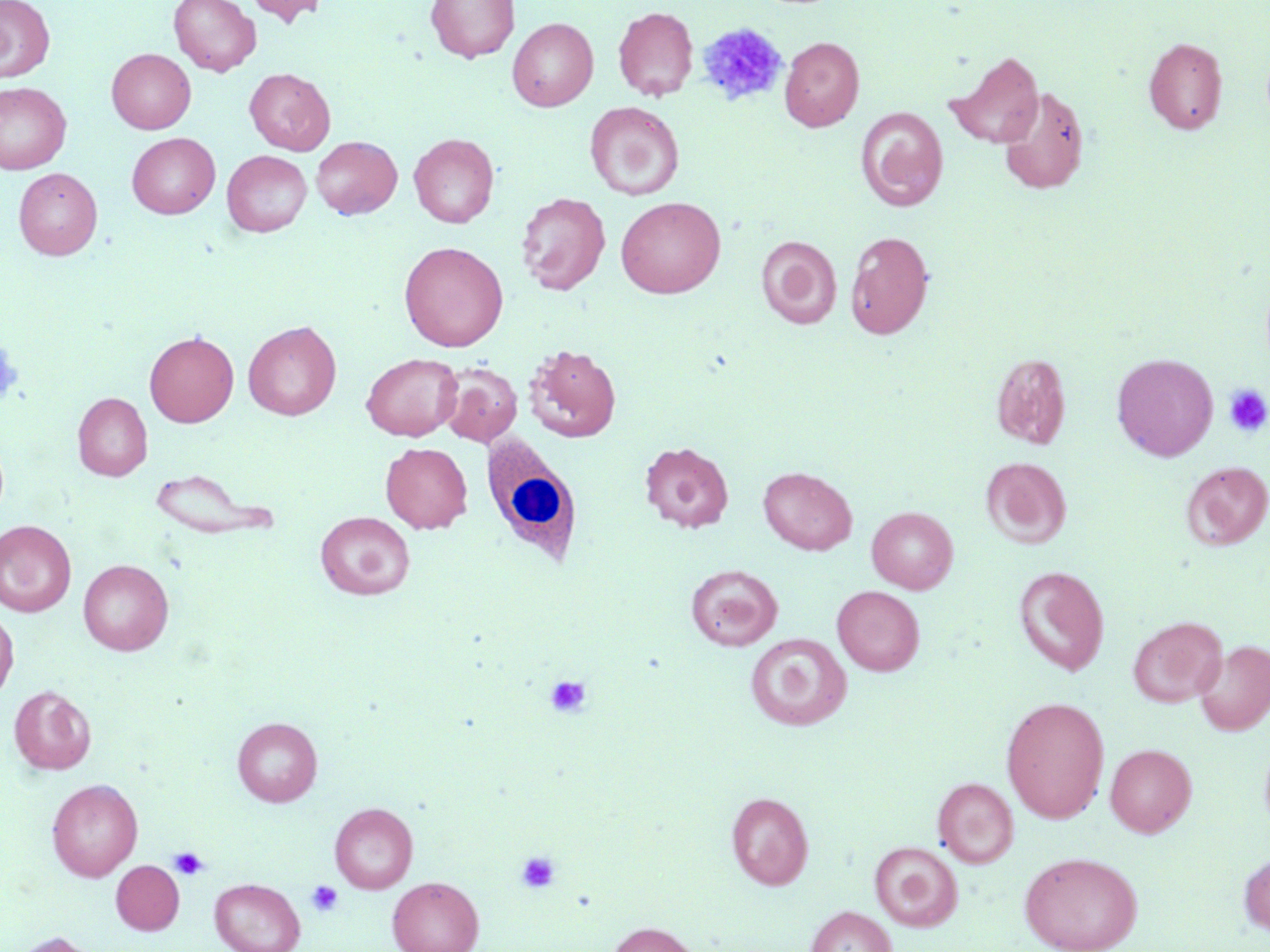
{
  "slide_level_diagnosis": "no evidence of blood parasites",
  "uninfected_red_blood_cell_locations": "approximate bounding boxes as named x1/y1/x2/y2 corners in pixels: (x1=0, y1=0, x2=55, y2=82), (x1=169, y1=0, x2=260, y2=76), (x1=246, y1=0, x2=329, y2=27), (x1=426, y1=0, x2=519, y2=62), (x1=613, y1=6, x2=698, y2=101), (x1=507, y1=17, x2=598, y2=111), (x1=780, y1=36, x2=864, y2=131), (x1=1143, y1=36, x2=1227, y2=134), (x1=107, y1=48, x2=195, y2=134), (x1=946, y1=51, x2=1044, y2=148), (x1=244, y1=68, x2=335, y2=155), (x1=0, y1=81, x2=72, y2=174), (x1=997, y1=85, x2=1090, y2=195), (x1=585, y1=101, x2=684, y2=200), (x1=856, y1=107, x2=948, y2=211), (x1=127, y1=133, x2=220, y2=218), (x1=409, y1=133, x2=499, y2=228), (x1=312, y1=136, x2=401, y2=219), (x1=222, y1=150, x2=312, y2=237), (x1=13, y1=167, x2=102, y2=260), (x1=516, y1=191, x2=610, y2=295), (x1=616, y1=196, x2=726, y2=298), (x1=846, y1=231, x2=934, y2=339), (x1=756, y1=236, x2=841, y2=328), (x1=399, y1=241, x2=508, y2=352), (x1=243, y1=320, x2=341, y2=420), (x1=144, y1=331, x2=239, y2=427), (x1=525, y1=344, x2=621, y2=442), (x1=362, y1=353, x2=462, y2=441), (x1=991, y1=353, x2=1071, y2=449), (x1=1112, y1=353, x2=1218, y2=461), (x1=438, y1=362, x2=522, y2=446), (x1=73, y1=392, x2=152, y2=481), (x1=640, y1=441, x2=733, y2=533), (x1=380, y1=442, x2=472, y2=533), (x1=980, y1=456, x2=1072, y2=547), (x1=1181, y1=461, x2=1270, y2=550), (x1=758, y1=466, x2=857, y2=555), (x1=148, y1=468, x2=279, y2=540), (x1=867, y1=506, x2=958, y2=593), (x1=315, y1=512, x2=415, y2=599), (x1=0, y1=521, x2=76, y2=616), (x1=78, y1=559, x2=173, y2=655), (x1=685, y1=564, x2=782, y2=651), (x1=1013, y1=566, x2=1109, y2=676), (x1=832, y1=585, x2=924, y2=675), (x1=0, y1=610, x2=18, y2=700), (x1=1128, y1=616, x2=1226, y2=707), (x1=745, y1=633, x2=851, y2=731), (x1=1194, y1=639, x2=1270, y2=736), (x1=9, y1=686, x2=95, y2=774), (x1=1001, y1=696, x2=1109, y2=823), (x1=233, y1=717, x2=322, y2=806), (x1=1105, y1=743, x2=1197, y2=837), (x1=933, y1=777, x2=1018, y2=867), (x1=47, y1=779, x2=142, y2=881), (x1=726, y1=791, x2=814, y2=889), (x1=330, y1=802, x2=418, y2=893), (x1=870, y1=841, x2=963, y2=931), (x1=1238, y1=850, x2=1270, y2=938), (x1=1019, y1=851, x2=1143, y2=952), (x1=110, y1=859, x2=185, y2=934), (x1=387, y1=876, x2=484, y2=952), (x1=210, y1=878, x2=305, y2=952), (x1=805, y1=905, x2=897, y2=952), (x1=607, y1=921, x2=702, y2=952), (x1=10, y1=932, x2=101, y2=952)",
  "image_size": "1270×952 pixels",
  "modality": "light microscopy",
  "platelet_locations": "approximate bounding boxes as named x1/y1/x2/y2 corners in pixels: (x1=696, y1=22, x2=788, y2=108), (x1=0, y1=337, x2=24, y2=409), (x1=1224, y1=384, x2=1270, y2=437), (x1=545, y1=675, x2=592, y2=718), (x1=169, y1=847, x2=209, y2=881), (x1=517, y1=851, x2=561, y2=893), (x1=306, y1=880, x2=343, y2=917)",
  "magnification": "1000x",
  "field_of_view": "single",
  "white_blood_cell_locations": "approximate bounding boxes as named x1/y1/x2/y2 corners in pixels: (x1=480, y1=436, x2=583, y2=566)",
  "preparation": "thin blood film",
  "stain": "May-Grünwald-Giemsa"
}